Report the malaria status of this cell.
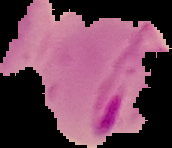
Parasitized.

preparation = thin blood smear
image size = 172×148 pixels
image type = segmented cell region on a black background